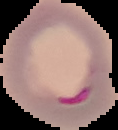
Summary:
  - Image type: segmented cell region with the area outside set to black
  - Result: malaria parasites detected
  - Image size: 118×130 pixels
  - Preparation: thin blood film